Assess this cell for malaria.
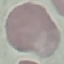
It is uninfected.

Thin blood film. Photographed with a smartphone camera at the microscope eyepiece. Automatically extracted cell patch, resized to 64 × 64 pixels. Giemsa-stained preparation.